Assess this cell for malaria.
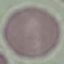
It is uninfected.

Cell patch, automatically extracted from a larger field of view and resized to 64 × 64 pixels. Acquired by smartphone through the microscope eyepiece. Giemsa-stained preparation. Thin blood film.